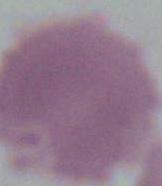

Summary:
  - Modality: photomicrograph
  - Magnification: 1000x
  - Identification: red blood cell